Identify the cell.
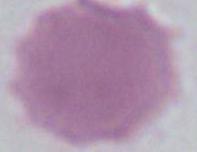
This is an erythrocyte.

Summary:
  - Magnification: 1000x
  - Modality: micrograph